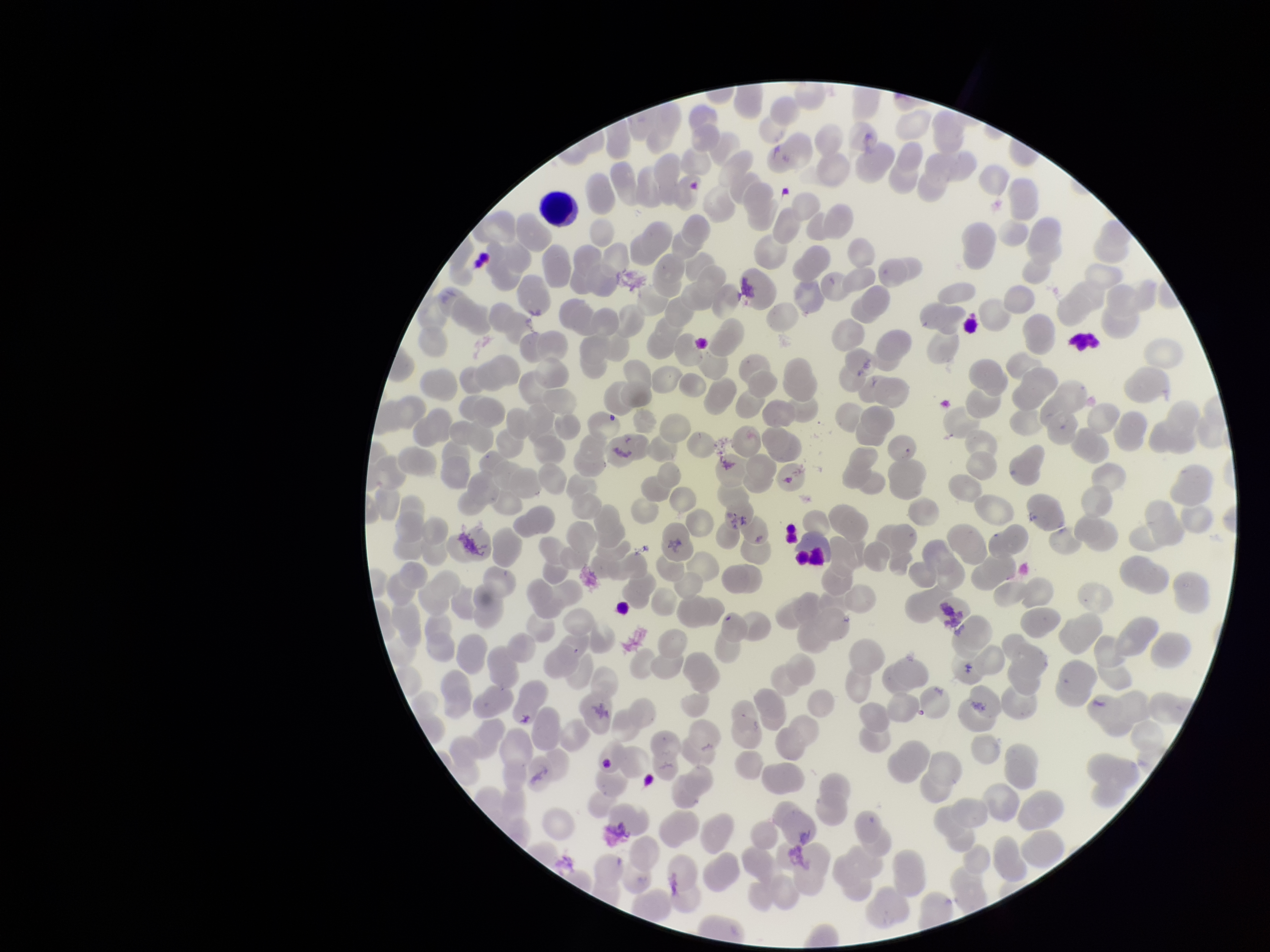

Summary:
  - Image size: 1270×952 pixels
  - Parasitized red blood cell count: 0
  - Field of view: single
  - Parasitized red blood cells: none detected
  - Species reported for this patient: Plasmodium falciparum
  - Red blood cell count: 269
  - Patient malaria status: positive
  - Preparation: thin blood smear
  - Stain: Giemsa
  - Capture: smartphone photograph through the microscope eyepiece